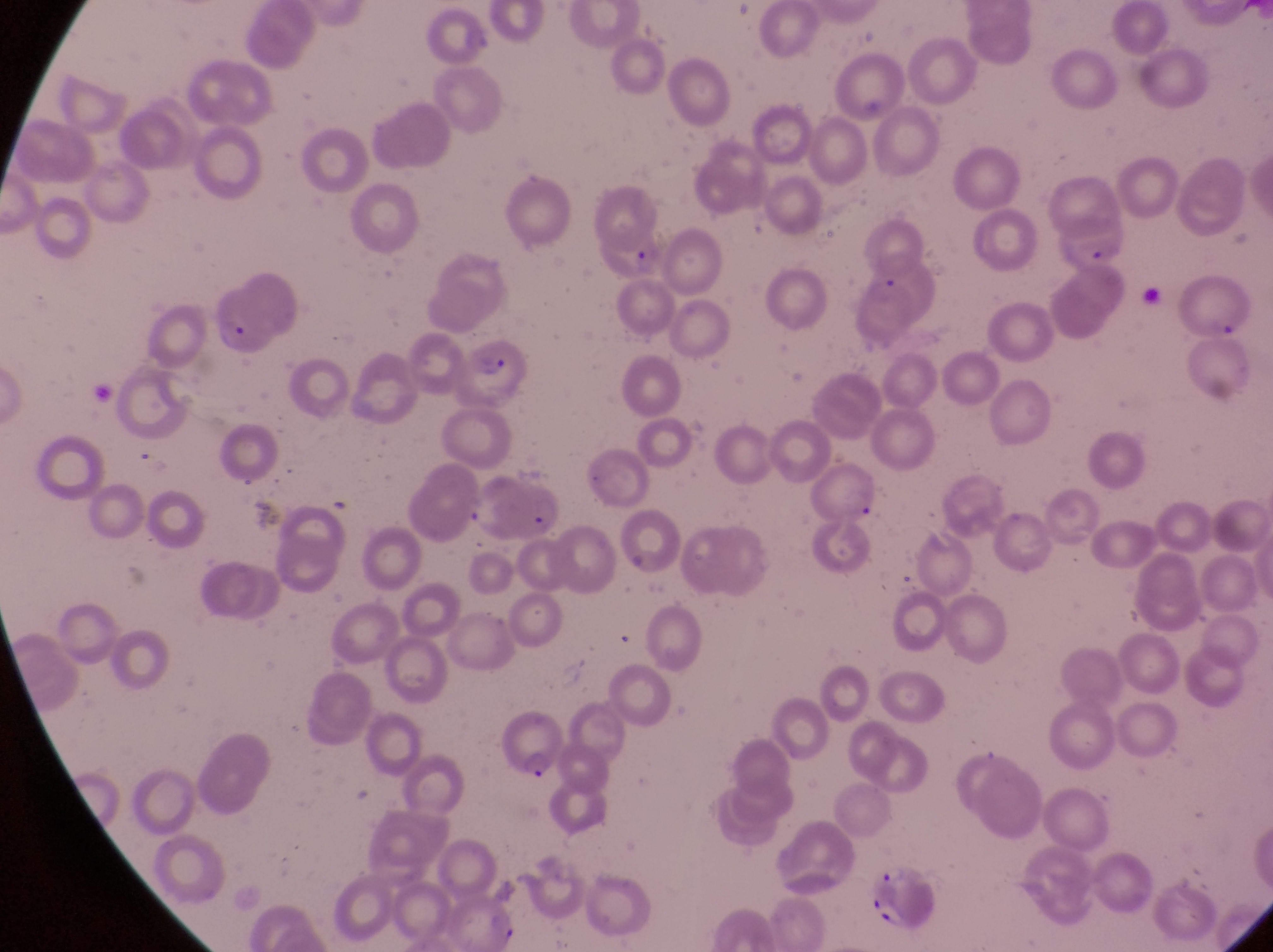
parasitised red blood cell locations = approximate bounding boxes as left top right bottom in pixels: 460 347 522 404; 500 714 569 786; 869 866 938 931
capture = smartphone photograph through the eyepiece of an Olympus CX-23 microscope
image size = 1273×952 pixels
field of view = single
preparation = thin blood film
magnification = 1000x
country = Uganda